Mark where platelets are.
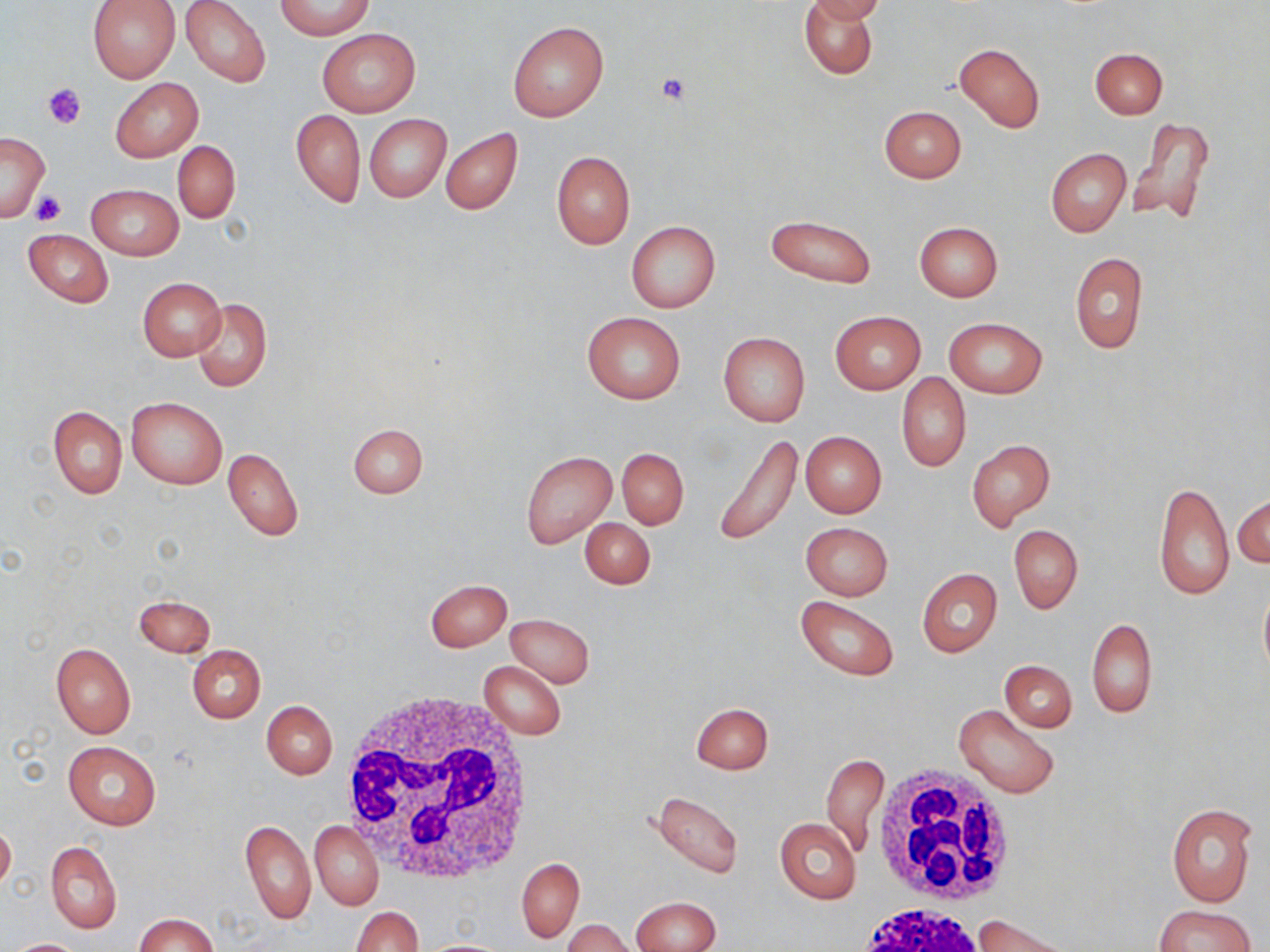
Approximate bounding boxes as named x1/y1/x2/y2 corners in pixels.
Platelets: (x1=656, y1=73, x2=690, y2=105), (x1=43, y1=82, x2=87, y2=128), (x1=32, y1=191, x2=67, y2=226).

Summary:
  - Uninfected red blood cell locations: (x1=88, y1=0, x2=180, y2=82), (x1=181, y1=0, x2=271, y2=87), (x1=799, y1=0, x2=878, y2=79), (x1=806, y1=0, x2=886, y2=23), (x1=276, y1=1, x2=373, y2=38), (x1=508, y1=20, x2=608, y2=122), (x1=317, y1=28, x2=420, y2=118), (x1=954, y1=44, x2=1045, y2=134), (x1=1090, y1=48, x2=1167, y2=119), (x1=110, y1=78, x2=202, y2=162), (x1=879, y1=105, x2=966, y2=183), (x1=290, y1=109, x2=365, y2=207), (x1=364, y1=114, x2=451, y2=202), (x1=1129, y1=116, x2=1217, y2=229), (x1=441, y1=128, x2=523, y2=215), (x1=1, y1=132, x2=49, y2=222), (x1=172, y1=141, x2=239, y2=222), (x1=1046, y1=148, x2=1131, y2=238), (x1=551, y1=150, x2=636, y2=250), (x1=86, y1=184, x2=183, y2=260), (x1=765, y1=214, x2=876, y2=288), (x1=625, y1=221, x2=721, y2=313), (x1=914, y1=221, x2=1003, y2=302), (x1=23, y1=229, x2=113, y2=307), (x1=1070, y1=251, x2=1148, y2=356), (x1=137, y1=277, x2=226, y2=361), (x1=192, y1=298, x2=271, y2=392), (x1=583, y1=311, x2=685, y2=404), (x1=829, y1=311, x2=925, y2=393), (x1=943, y1=316, x2=1047, y2=398), (x1=718, y1=332, x2=810, y2=426), (x1=896, y1=373, x2=970, y2=473), (x1=126, y1=397, x2=228, y2=489), (x1=48, y1=405, x2=127, y2=499), (x1=348, y1=422, x2=427, y2=500), (x1=713, y1=431, x2=804, y2=549), (x1=800, y1=431, x2=887, y2=517), (x1=966, y1=438, x2=1055, y2=529), (x1=223, y1=448, x2=304, y2=541), (x1=617, y1=448, x2=689, y2=529), (x1=520, y1=450, x2=617, y2=549), (x1=1153, y1=480, x2=1234, y2=600), (x1=1233, y1=493, x2=1270, y2=570), (x1=580, y1=516, x2=654, y2=589), (x1=799, y1=521, x2=893, y2=601), (x1=1008, y1=525, x2=1082, y2=614), (x1=917, y1=567, x2=1002, y2=658), (x1=425, y1=579, x2=512, y2=651), (x1=1258, y1=584, x2=1270, y2=682), (x1=133, y1=594, x2=216, y2=656), (x1=795, y1=596, x2=899, y2=680), (x1=505, y1=614, x2=594, y2=687), (x1=1086, y1=618, x2=1156, y2=718), (x1=51, y1=643, x2=135, y2=738), (x1=188, y1=645, x2=265, y2=724), (x1=999, y1=660, x2=1077, y2=732), (x1=478, y1=661, x2=568, y2=738), (x1=261, y1=700, x2=338, y2=779), (x1=691, y1=702, x2=773, y2=774), (x1=953, y1=704, x2=1060, y2=799), (x1=63, y1=741, x2=162, y2=830), (x1=822, y1=752, x2=889, y2=857), (x1=651, y1=790, x2=743, y2=880), (x1=1165, y1=802, x2=1258, y2=908), (x1=240, y1=817, x2=316, y2=925), (x1=775, y1=818, x2=862, y2=903), (x1=309, y1=819, x2=383, y2=910), (x1=0, y1=821, x2=15, y2=893), (x1=46, y1=842, x2=121, y2=933), (x1=517, y1=858, x2=583, y2=941), (x1=631, y1=897, x2=721, y2=952), (x1=1153, y1=904, x2=1255, y2=952), (x1=350, y1=906, x2=421, y2=952), (x1=135, y1=913, x2=218, y2=951), (x1=973, y1=915, x2=1070, y2=952), (x1=563, y1=919, x2=635, y2=952), (x1=4, y1=938, x2=88, y2=952), (x1=418, y1=939, x2=514, y2=951)
  - White blood cell locations: (x1=337, y1=688, x2=540, y2=885), (x1=875, y1=765, x2=1018, y2=906), (x1=851, y1=903, x2=990, y2=952)
  - Slide-level diagnosis: negative for blood parasites
  - Image size: 1270×952 pixels
  - Magnification: 1000x
  - Field of view: one of a larger specimen
  - Modality: optical microscopy
  - Preparation: thin blood film
  - Stain: May-Grünwald-Giemsa